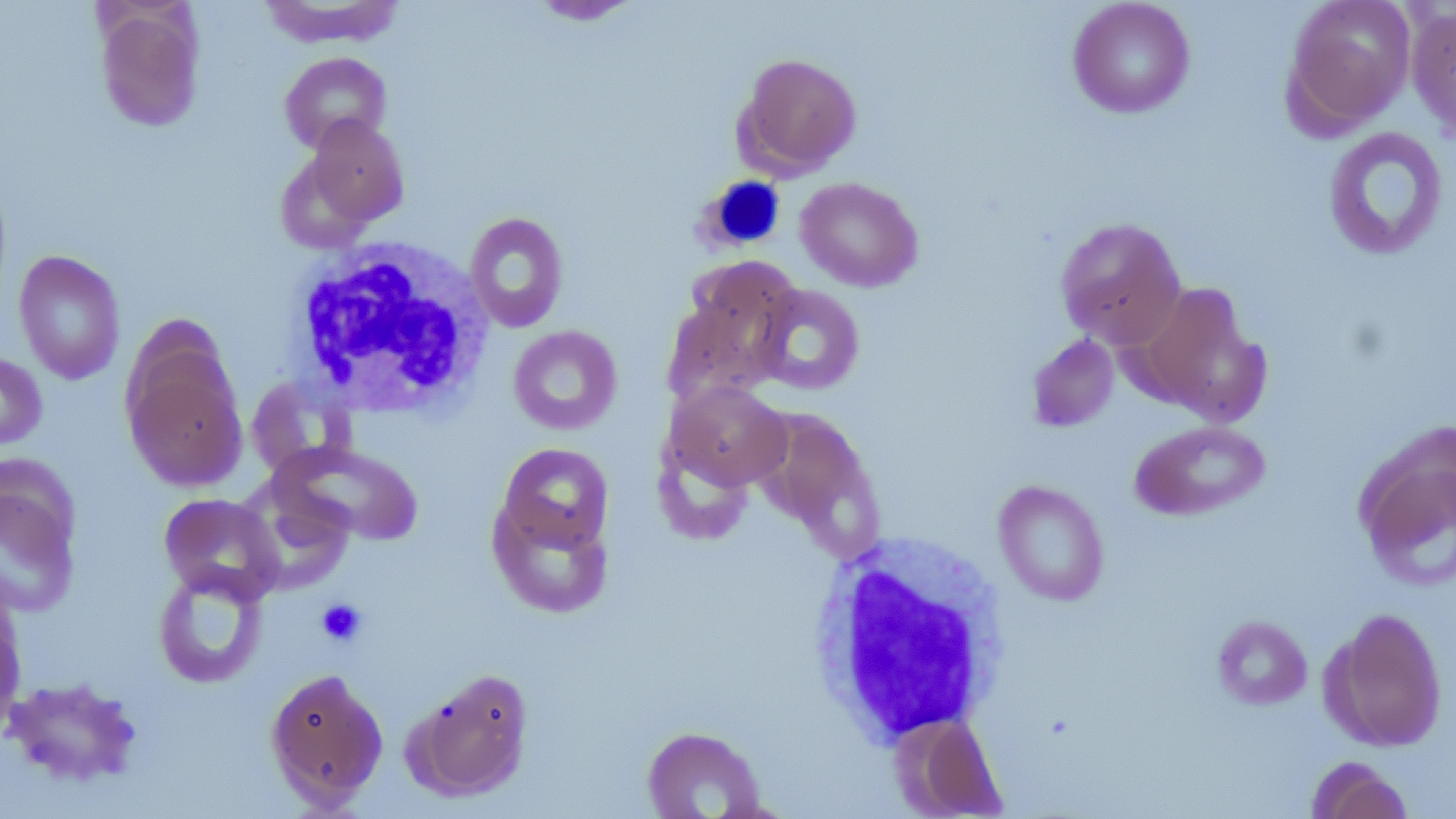 Approximate bounding boxes as (x1,y1)-(x2,y2) corner pairs in pixels. Uninfected red blood cell locations: (528,0)-(643,26), (1066,0)-(1196,119), (1283,0)-(1417,133), (256,1)-(406,48), (1406,4)-(1456,145), (96,6)-(205,132), (279,51)-(392,154), (734,52)-(863,177), (302,116)-(409,228), (1322,126)-(1449,261), (794,176)-(924,292), (464,212)-(569,333), (1054,216)-(1187,350), (13,250)-(127,385), (663,270)-(797,408), (1134,282)-(1269,423), (752,283)-(865,396), (507,325)-(623,435), (122,332)-(247,493), (1025,334)-(1119,432), (0,353)-(48,452), (245,376)-(358,481), (663,380)-(791,491), (751,406)-(884,555), (1129,419)-(1271,521), (1354,434)-(1456,592), (275,442)-(424,546), (494,442)-(615,561), (0,473)-(83,618), (992,479)-(1110,606), (487,491)-(615,618), (159,493)-(283,603), (152,565)-(269,689), (0,584)-(26,734), (1323,607)-(1449,752), (1212,615)-(1314,709), (264,666)-(389,809), (404,667)-(535,803), (2,676)-(144,787), (894,713)-(1007,818), (640,725)-(768,819), (1305,755)-(1415,819). White blood cell locations: (697,175)-(788,254), (288,237)-(494,418), (807,533)-(1013,747). Platelet locations: (317,598)-(367,647). Slide-level diagnosis: no evidence of blood parasites. Optical microscopy. Thin blood smear. Captured at 1000x magnification. May-Grünwald-Giemsa stain. Single field of view. Image is 1456×819 pixels.